Name the parasite shown.
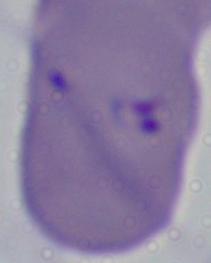

Babesia.

{
  "modality": "micrograph",
  "magnification": "1000x"
}